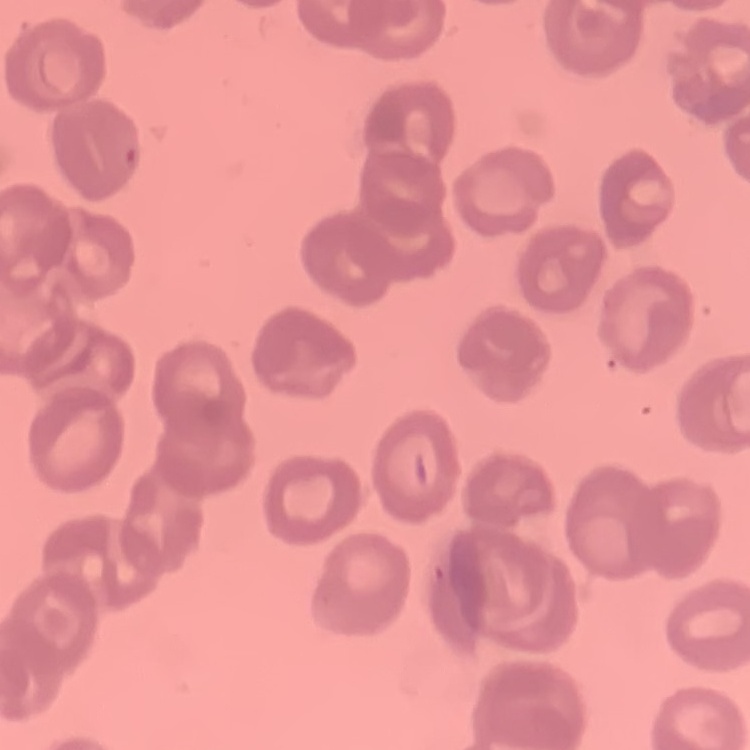
Summary:
  - Erythrocyte morphology: no rouleaux formation
  - Stain: Field's or Giemsa
  - Preparation: thin peripheral smear
  - Image type: one tile cut from a larger photomicrograph